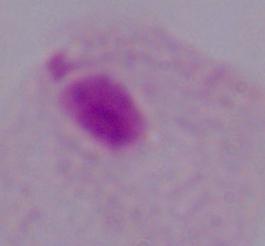

Summary:
  - Modality: photomicrograph
  - Identification: trichomonad
  - Magnification: 1000x